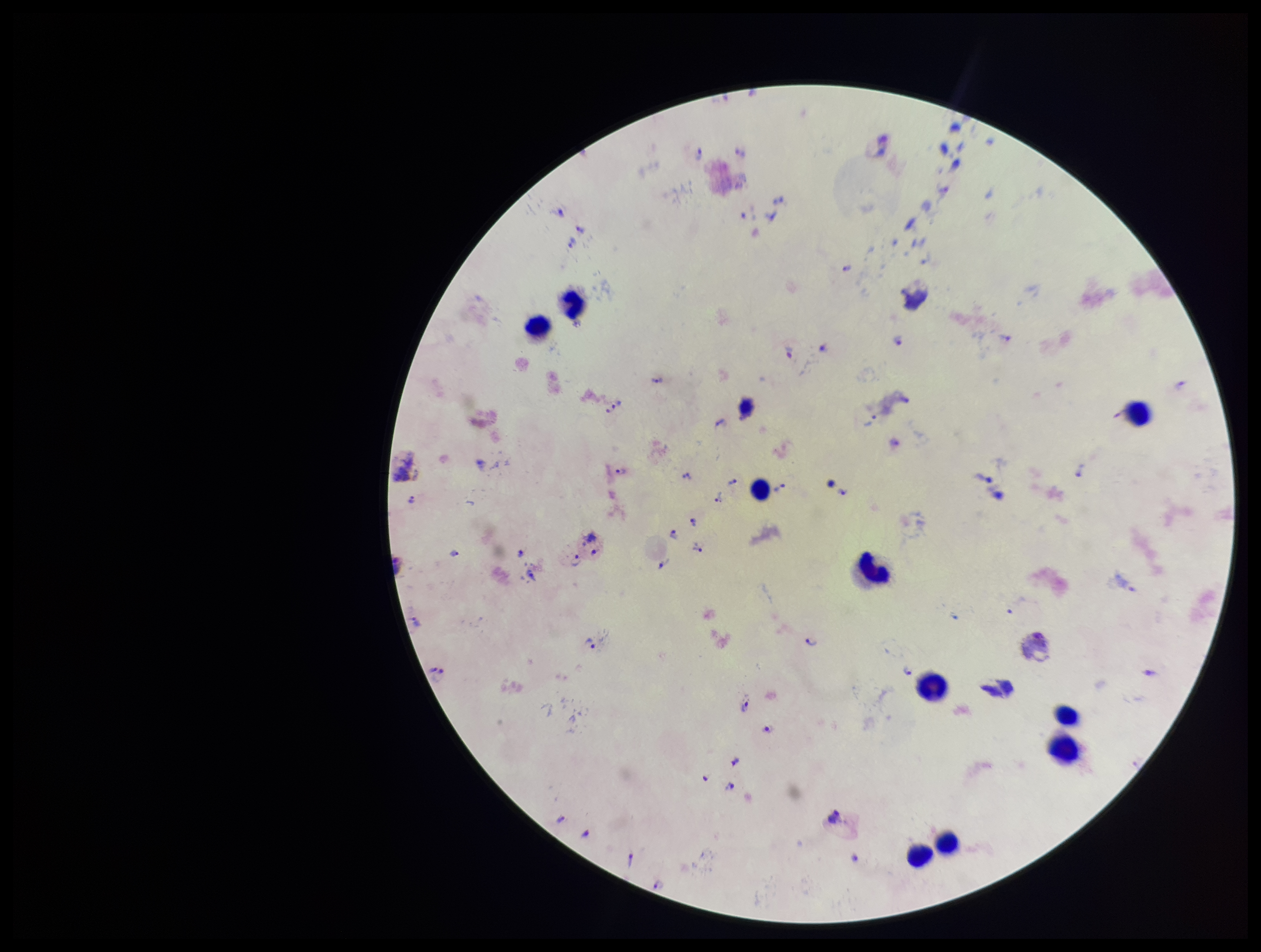

Summary:
  - Preparation: thick smear
  - Stain: Giemsa
  - Capture: smartphone photograph through the microscope eyepiece
  - Image size: 1261×952 pixels
  - Parasite count: 47
  - Field of view: one from this slide
  - Plasmodium parasites: seen
  - Species reported for this patient: Plasmodium vivax
  - Patient malaria status: positive
  - Leukocyte count: 10